Identify the preparation type.
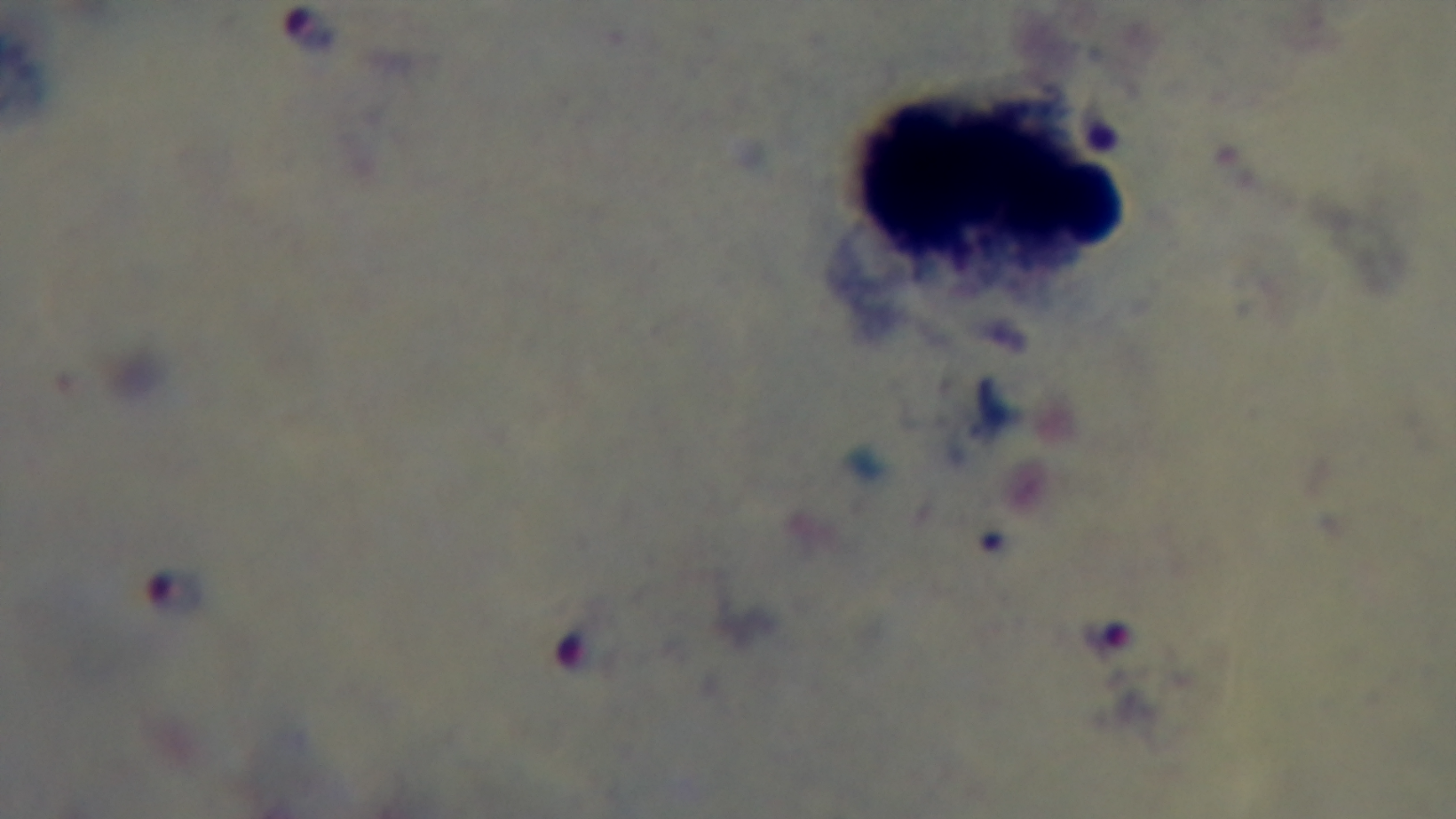

It is a thick blood film.

{
  "objective": "100x oil immersion",
  "stain": "Giemsa",
  "malaria_status": "infected",
  "field_of_view": "single",
  "capture": "mounted 4K digital camera",
  "modality": "light microscopy"
}